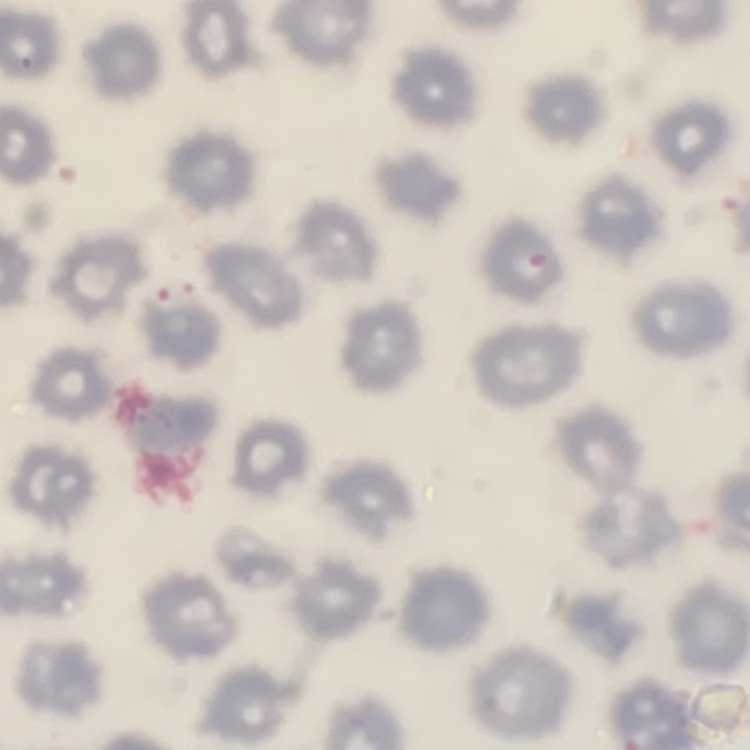

Summary:
  - Red blood cell morphology: no rouleaux formation
  - Image type: one tile cut from a larger photomicrograph
  - Stain: Field's or Giemsa
  - Preparation: thin peripheral smear